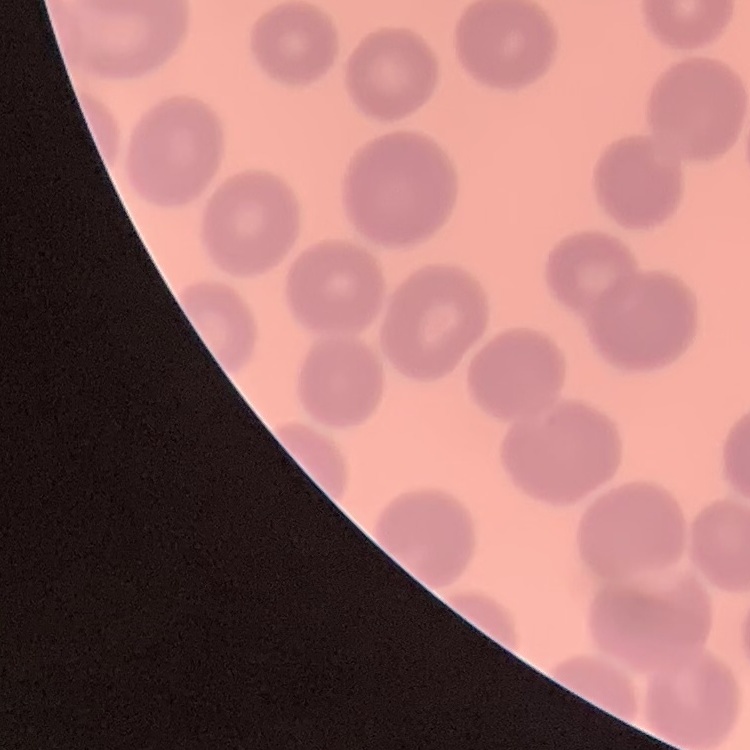

The erythrocytes show no rouleaux formation. Thin blood smear. One tile cut from a larger photomicrograph. Stained with either Field's or Giemsa.